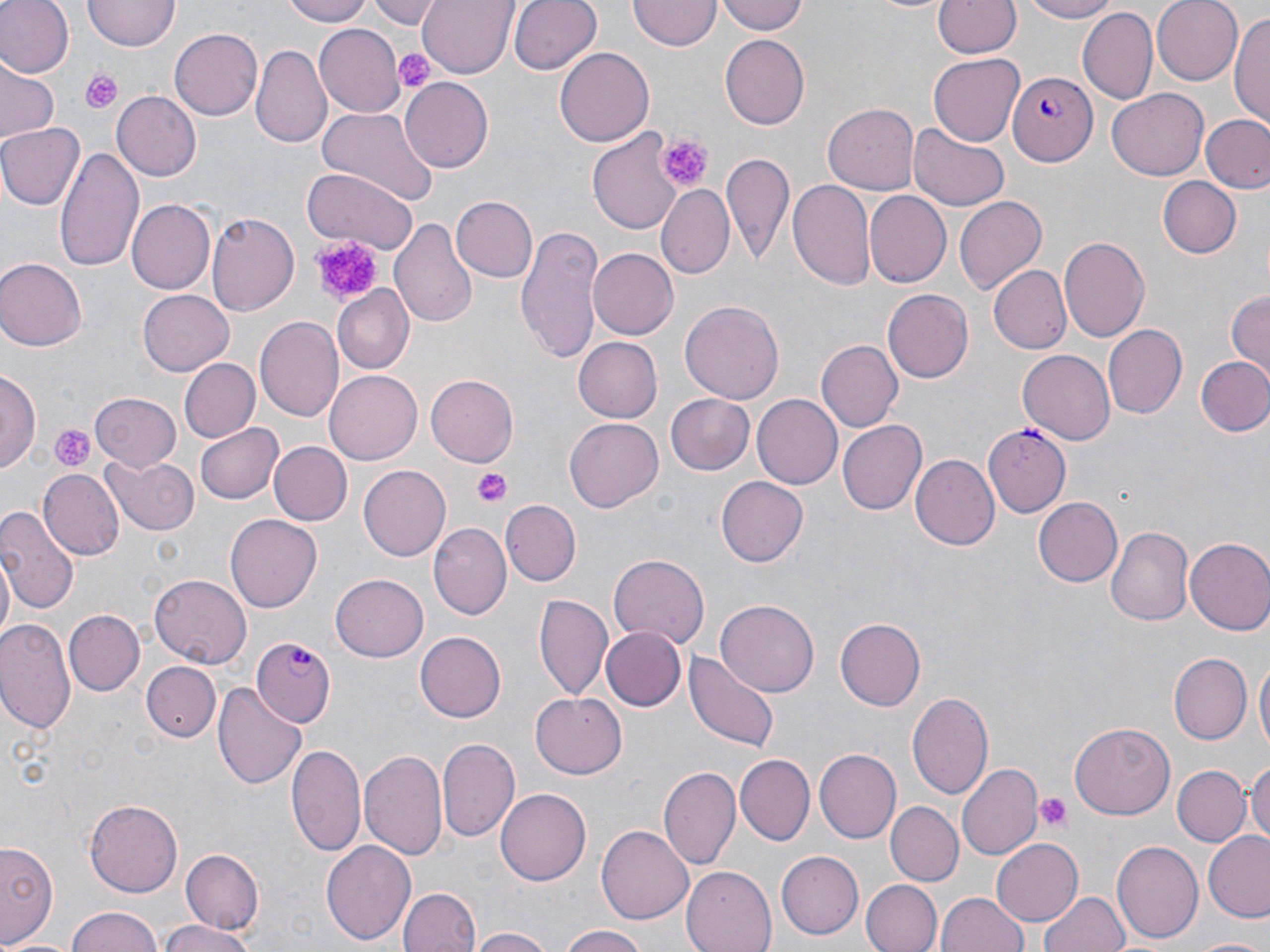

{
  "slide_level_diagnosis": "Plasmodium falciparum",
  "platelet_locations": "approximate bounding boxes as (x1,y1)-(x2,y2) corner pairs in pixels: (395,48)-(436,92), (82,69)-(123,115), (653,132)-(714,191), (308,235)-(389,306), (47,421)-(97,473), (476,470)-(511,508), (1034,792)-(1074,834)",
  "plasmodium_falciparum_infected_red_blood_cell_locations": "approximate bounding boxes as (x1,y1)-(x2,y2) corner pairs in pixels: (1009,70)-(1099,169), (983,424)-(1071,517), (250,637)-(336,725)",
  "modality": "light microscopy",
  "image_size": "1270×952 pixels",
  "stain": "May-Grünwald-Giemsa",
  "magnification": "1000x",
  "field_of_view": "single",
  "uninfected_red_blood_cell_locations": "approximate bounding boxes as (x1,y1)-(x2,y2) corner pairs in pixels: (0,0)-(73,78), (281,0)-(375,26), (366,0)-(445,26), (418,0)-(517,75), (510,0)-(601,75), (716,0)-(808,36), (1018,0)-(1125,23), (1151,0)-(1243,84), (629,1)-(718,52), (933,1)-(1020,60), (83,2)-(178,52), (1077,8)-(1158,105), (1232,11)-(1270,132), (313,24)-(405,119), (168,28)-(263,122), (721,36)-(809,129), (251,44)-(332,147), (554,48)-(653,145), (930,54)-(1024,144), (0,58)-(60,144), (401,77)-(493,173), (1108,87)-(1211,179), (110,90)-(201,181), (825,102)-(922,194), (313,105)-(438,206), (1202,115)-(1270,193), (0,123)-(84,210), (909,124)-(1009,210), (589,130)-(687,235), (54,149)-(143,271), (720,150)-(794,259), (301,168)-(417,250), (1156,176)-(1241,259), (787,178)-(879,293), (656,185)-(734,280), (864,191)-(950,286), (452,195)-(538,281), (955,196)-(1044,291), (125,200)-(213,294), (207,213)-(302,317), (391,215)-(478,330), (518,226)-(604,361), (1058,235)-(1149,343), (586,246)-(678,340), (0,257)-(86,351), (990,265)-(1072,355), (330,285)-(415,374), (137,287)-(233,374), (1227,287)-(1270,375), (882,290)-(972,383), (680,299)-(783,404), (255,316)-(344,422), (1104,324)-(1186,420), (573,337)-(662,423), (818,340)-(902,431), (1017,350)-(1116,445), (1196,354)-(1270,437), (180,359)-(258,441), (1,370)-(39,474), (326,371)-(421,464), (426,375)-(518,466), (89,392)-(183,471), (668,393)-(754,475), (753,394)-(842,489), (565,417)-(663,512), (837,419)-(926,515), (195,422)-(285,505), (268,440)-(352,525), (103,454)-(199,536), (913,455)-(1000,549), (359,465)-(450,561), (40,468)-(123,559), (716,476)-(808,565), (1034,497)-(1123,585), (502,502)-(580,586), (0,503)-(79,617), (226,511)-(323,612), (426,521)-(511,617), (1106,526)-(1193,626), (1184,538)-(1270,634), (1,553)-(15,646), (608,554)-(709,649), (149,572)-(251,666), (330,575)-(429,662), (536,592)-(612,700), (717,600)-(818,698), (63,610)-(143,694), (1,617)-(77,737), (835,619)-(924,712), (600,626)-(685,711), (415,631)-(506,721), (685,651)-(779,753), (1170,653)-(1251,744), (1255,660)-(1269,762), (142,663)-(221,741), (214,680)-(309,791), (907,691)-(994,800), (530,692)-(628,778), (1070,722)-(1175,820), (437,739)-(518,841), (288,741)-(368,860), (360,747)-(449,864), (814,748)-(902,842), (735,754)-(813,845), (1247,760)-(1270,850), (957,763)-(1041,860), (659,765)-(739,871), (1172,765)-(1249,846), (497,788)-(591,885), (84,799)-(183,898), (887,802)-(961,884), (597,823)-(693,924), (1202,833)-(1270,921), (991,838)-(1083,927), (0,840)-(59,949), (321,840)-(416,945), (1112,841)-(1204,943), (177,849)-(264,936), (776,852)-(863,940), (682,863)-(781,952), (861,877)-(941,952), (399,887)-(479,952), (1042,891)-(1131,952), (935,892)-(1028,952), (67,908)-(165,952), (156,919)-(256,952), (557,924)-(647,952), (467,927)-(559,952), (1188,936)-(1270,952)",
  "preparation": "thin blood film"
}